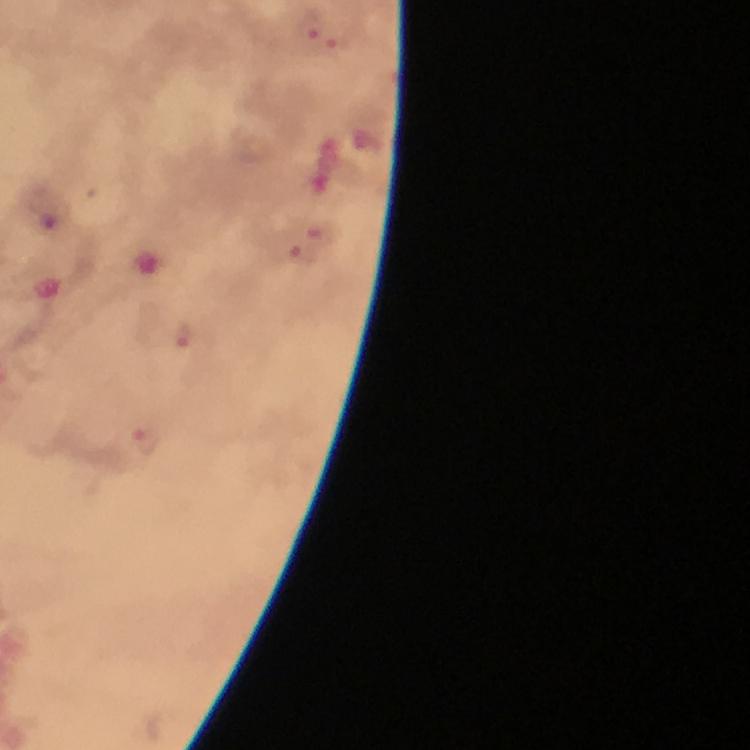

Approximate centers as (x, y) in pixels. Plasmodium parasite locations: (309, 27), (339, 44), (50, 209), (321, 231), (303, 250), (183, 335), (146, 442). Image is 750×750 pixels. From a diagnostic examination for malaria. Giemsa stain. Cropped region of a single field of view. 100x magnification. Thick blood smear. Immersion oil applied. Photographed with a smartphone mounted on the microscope.